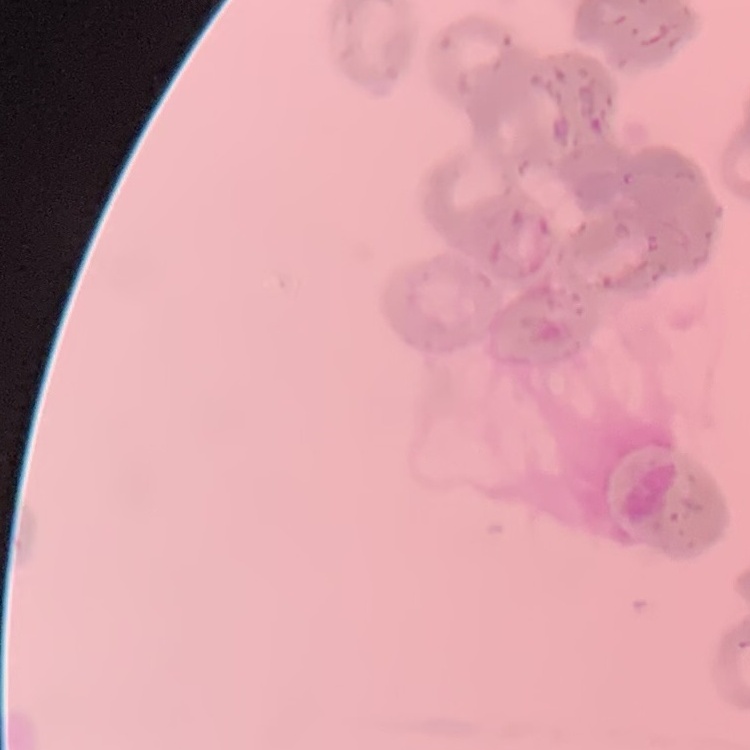

red blood cell morphology = rouleaux formation
stain = Field's or Giemsa
image type = one tile cut from a larger photomicrograph
preparation = thin blood film